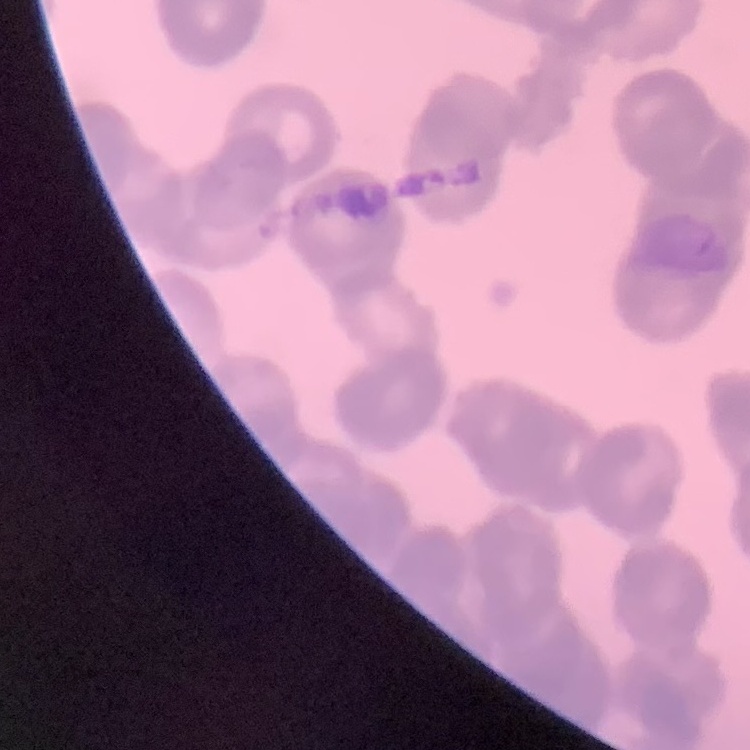
Summary:
  - Erythrocyte morphology: rouleaux formation
  - Preparation: thin blood film
  - Image type: square crop of a larger photomicrograph
  - Stain: Field's or Giemsa